Locate every blood parasite and identify its species.
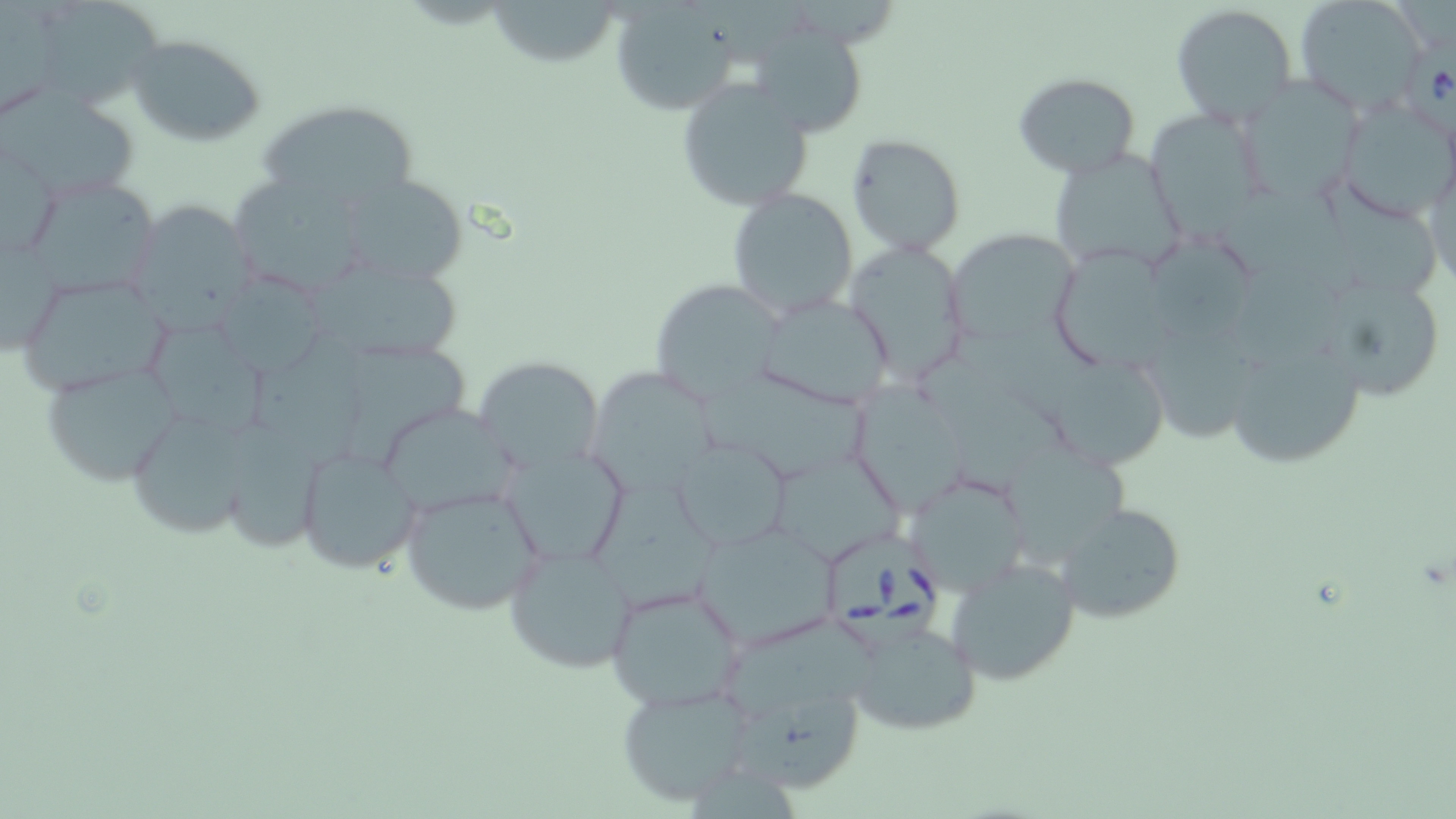

Approximate bounding boxes as (x1, y1, x2, y2) in pixels.
Babesia divergens-infected red blood cells: (1405, 42, 1456, 138), (826, 536, 946, 658).
No Plasmodium falciparum, Plasmodium ovale, Plasmodium malariae, Plasmodium vivax, or Trypanosoma brucei observed.

Summary:
  - Uninfected red blood cell locations: (29, 0, 164, 113), (488, 0, 623, 70), (1295, 0, 1428, 116), (608, 4, 742, 116), (1169, 4, 1299, 125), (704, 6, 814, 75), (753, 31, 862, 129), (127, 33, 267, 147), (1013, 71, 1141, 179), (676, 76, 814, 210), (1236, 81, 1358, 202), (4, 87, 143, 200), (1332, 98, 1456, 223), (259, 99, 417, 216), (1144, 110, 1268, 229), (845, 133, 965, 256), (1, 139, 61, 264), (1048, 147, 1188, 275), (1422, 152, 1456, 291), (339, 172, 470, 285), (23, 173, 162, 300), (227, 173, 378, 299), (1324, 181, 1438, 301), (725, 188, 859, 318), (125, 199, 259, 329), (1, 228, 63, 358), (944, 228, 1079, 346), (1149, 236, 1263, 346), (841, 239, 972, 384), (1051, 245, 1171, 378), (313, 256, 465, 366), (211, 273, 333, 377), (14, 274, 175, 397), (648, 278, 787, 408), (1335, 285, 1442, 399), (749, 291, 897, 412), (1146, 318, 1253, 451), (144, 321, 275, 435), (1219, 321, 1371, 472), (253, 337, 380, 475), (343, 346, 467, 473), (914, 348, 1074, 498), (474, 356, 603, 475), (1049, 357, 1164, 477), (38, 362, 185, 488), (585, 364, 724, 495), (698, 365, 873, 479), (849, 381, 972, 514), (375, 401, 521, 518), (123, 408, 262, 536), (230, 419, 337, 558), (769, 438, 907, 573), (671, 439, 792, 553), (1002, 444, 1134, 562), (294, 445, 425, 575), (502, 447, 629, 566), (905, 471, 1029, 596), (399, 481, 546, 617), (590, 487, 724, 613), (1053, 502, 1185, 624), (694, 521, 840, 647), (504, 540, 639, 671), (944, 555, 1082, 686), (604, 582, 748, 712), (843, 615, 983, 738), (721, 622, 876, 723), (615, 682, 755, 806), (741, 691, 862, 797), (688, 772, 804, 819)
  - Slide-level diagnosis: Babesia divergens
  - Image size: 1456×819 pixels
  - Field of view: one of a larger specimen
  - Stain: May-Grünwald-Giemsa
  - Magnification: 1000x
  - Modality: light microscopy
  - Preparation: thin blood smear